Name the blood parasite species.
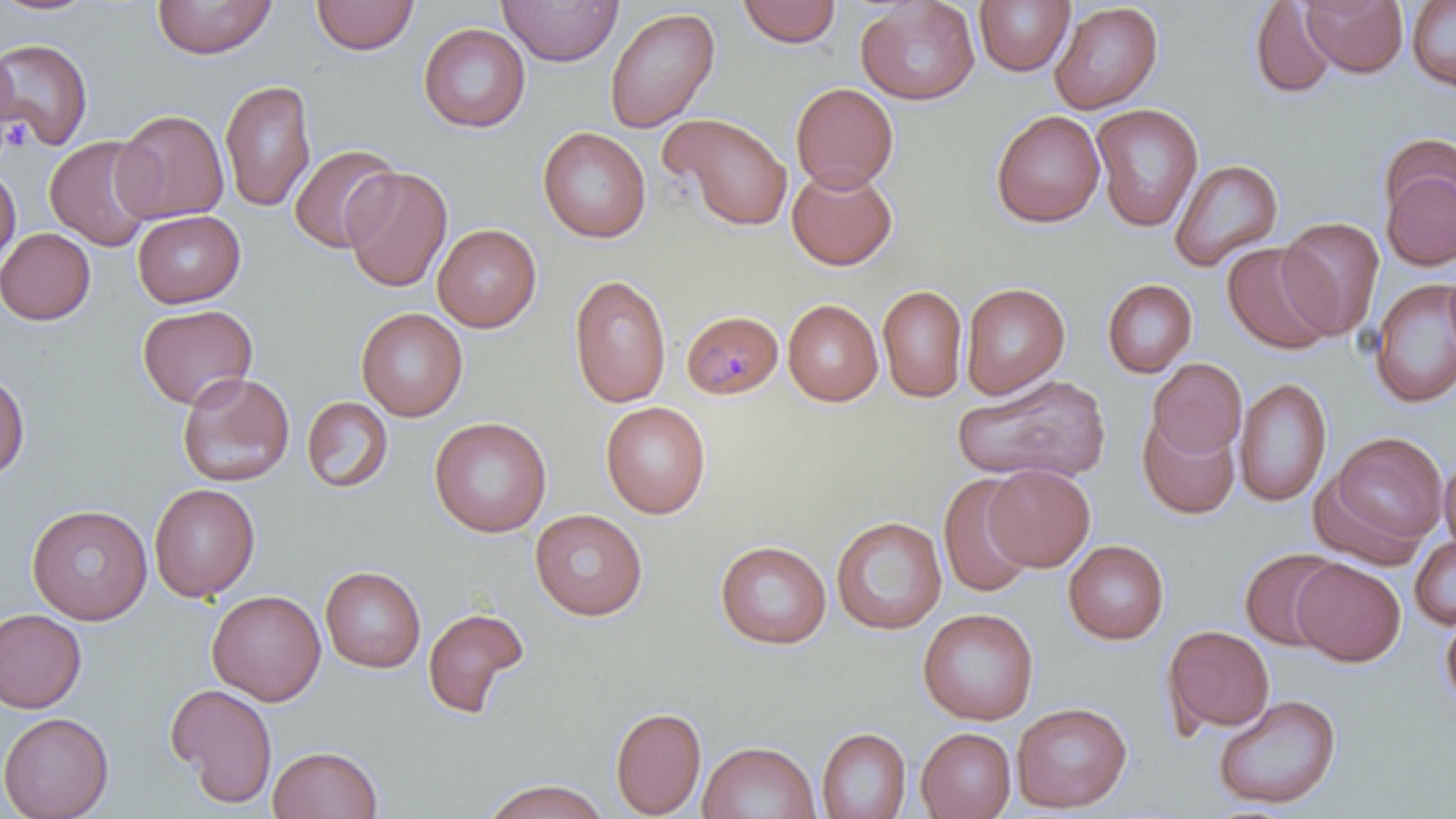

Plasmodium malariae.

Summary:
  - Coordinate format: approximate bounding boxes as [x1, y1, x2, y2] in pixels
  - Platelet locations: [2, 116, 32, 154]
  - Plasmodium malariae-infected red blood cell locations: [682, 310, 783, 399]
  - Uninfected red blood cell locations: [151, 0, 277, 59], [310, 0, 419, 55], [498, 0, 623, 66], [1301, 0, 1408, 78], [1406, 0, 1456, 94], [0, 1, 99, 17], [736, 1, 842, 48], [855, 1, 980, 107], [974, 1, 1074, 76], [1249, 1, 1339, 100], [1050, 2, 1164, 114], [604, 7, 720, 133], [418, 22, 531, 133], [0, 39, 94, 151], [0, 46, 19, 137], [219, 79, 316, 213], [790, 82, 899, 192], [1091, 103, 1203, 233], [112, 109, 229, 224], [991, 110, 1105, 228], [658, 112, 794, 231], [537, 126, 652, 243], [44, 136, 158, 251], [288, 143, 402, 253], [1379, 149, 1456, 271], [1168, 159, 1284, 272], [0, 165, 21, 269], [342, 167, 452, 294], [786, 167, 898, 270], [132, 209, 245, 308], [1277, 217, 1384, 340], [432, 223, 542, 332], [0, 227, 96, 325], [1221, 241, 1339, 355], [568, 273, 672, 408], [1369, 277, 1456, 409], [1101, 279, 1197, 377], [960, 282, 1070, 399], [877, 284, 968, 403], [782, 299, 884, 406], [137, 304, 258, 410], [355, 307, 468, 422], [1147, 357, 1246, 459], [0, 368, 30, 484], [177, 371, 295, 488], [953, 374, 1111, 484], [1235, 377, 1332, 507], [301, 396, 393, 493], [600, 401, 711, 519], [1137, 414, 1241, 519], [429, 416, 552, 538], [1325, 431, 1448, 549], [1440, 456, 1456, 557], [983, 463, 1095, 571], [937, 474, 1037, 598], [149, 483, 260, 602], [26, 503, 152, 625], [530, 509, 648, 620], [831, 516, 946, 635], [1410, 536, 1456, 630], [715, 540, 832, 650], [1063, 540, 1169, 645], [1239, 547, 1345, 651], [1292, 559, 1405, 666], [320, 566, 426, 673], [207, 590, 326, 705], [421, 606, 531, 720], [0, 608, 87, 714], [918, 608, 1038, 725], [1439, 609, 1456, 712], [1162, 624, 1275, 735], [166, 683, 279, 808], [1212, 693, 1342, 811], [1012, 701, 1133, 812], [610, 705, 707, 819], [0, 711, 115, 819], [817, 727, 911, 818], [916, 727, 1016, 819], [698, 740, 820, 819], [268, 745, 383, 818], [481, 778, 610, 819]
  - Image size: 1456×819 pixels
  - Preparation: thin blood film
  - Modality: optical microscopy
  - Field of view: one of a larger specimen
  - Stain: May-Grünwald-Giemsa
  - Magnification: 1000x